Describe the morphology of the red blood cells.
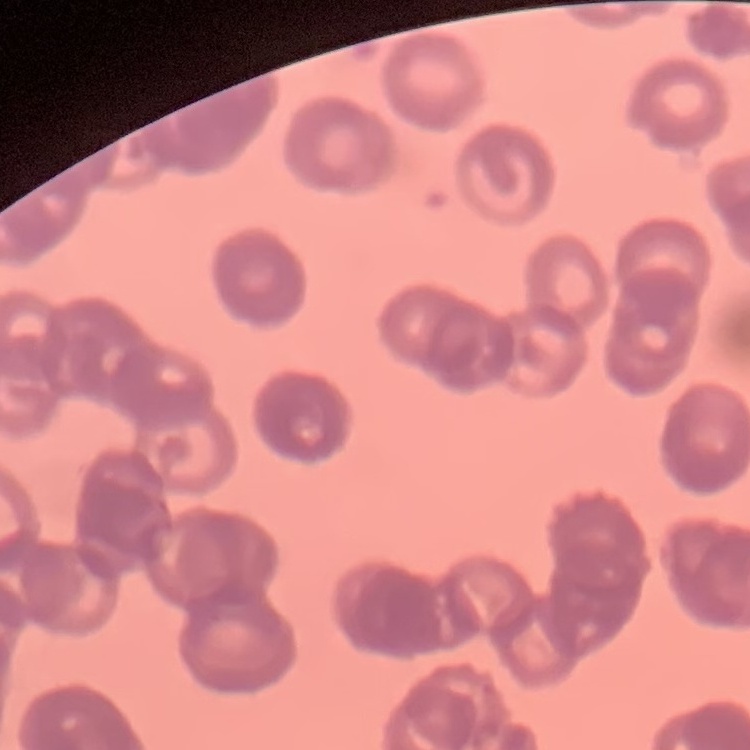

They show rouleaux formation.

Square crop of a larger photomicrograph. Thin blood smear. Field's or Giemsa stain.